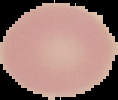 Malaria status: uninfected. From a thin blood film. Image is 118×100 pixels. Segmented cell region on a black background.